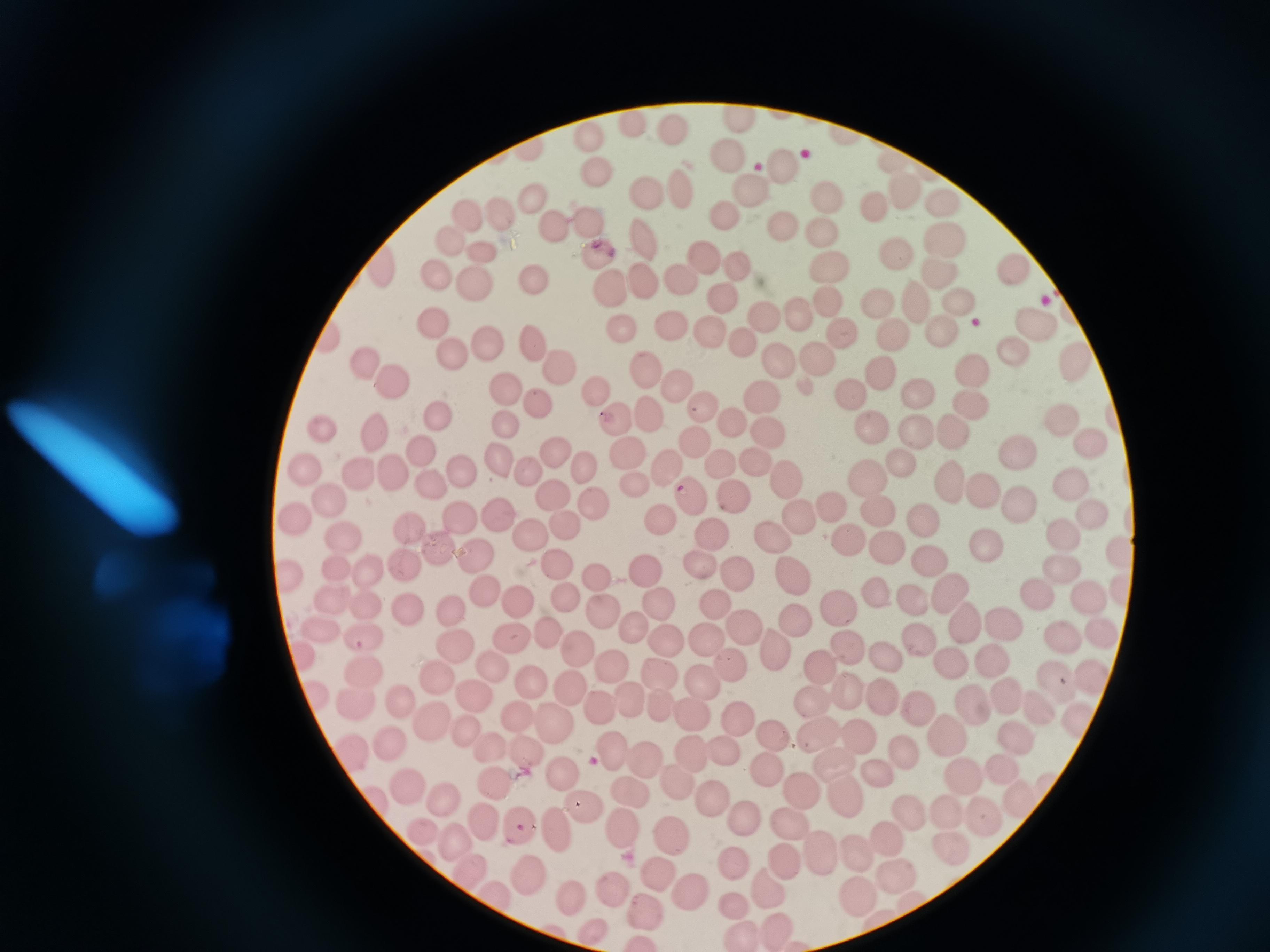

Approximate centers as [x, y] in pixels. Cell locations: [742, 117], [628, 125], [670, 127], [590, 133], [730, 157], [889, 159], [786, 165], [594, 173], [680, 188], [823, 190], [648, 192], [748, 193], [904, 196], [937, 197], [530, 200], [874, 205], [496, 214], [725, 216], [463, 218], [586, 223], [783, 223], [551, 224], [824, 230], [948, 237], [640, 239], [451, 240], [600, 254], [895, 255], [706, 256], [483, 257], [1017, 264], [382, 266], [826, 270], [435, 271], [738, 271], [943, 272], [677, 273], [470, 284], [538, 286], [645, 286], [611, 288], [723, 299], [956, 299], [827, 301], [918, 301], [874, 302], [795, 311], [771, 319], [672, 321], [1037, 321], [433, 325], [622, 325], [944, 329], [843, 331], [713, 332], [891, 334], [330, 340], [486, 341], [750, 341], [532, 345], [1012, 349], [447, 354], [778, 363], [819, 364], [369, 365], [971, 365], [641, 366], [1080, 366], [558, 369], [883, 373], [391, 379], [676, 382], [507, 387], [596, 388], [921, 391], [855, 394], [762, 396], [539, 404], [972, 407], [701, 411], [652, 413], [437, 417], [734, 417], [621, 419], [1063, 423], [507, 427], [920, 427], [873, 428], [952, 429], [329, 432], [375, 433], [766, 435], [692, 438], [1089, 440], [553, 449], [426, 451], [626, 452], [1017, 455], [500, 456], [582, 465], [759, 465], [905, 465], [668, 467], [723, 469], [308, 471], [394, 471], [523, 473], [466, 474], [361, 476], [870, 477], [784, 479], [952, 480], [435, 481], [1077, 484], [638, 485], [986, 492], [554, 494], [690, 495], [732, 497], [325, 499], [1018, 499], [594, 503], [833, 505], [880, 509], [800, 515], [1091, 515], [503, 518], [460, 519], [929, 520], [661, 521], [296, 522], [565, 528], [408, 530], [772, 533], [848, 535], [341, 537], [710, 538], [1066, 538], [536, 539], [436, 545], [890, 548], [1121, 549], [993, 552], [476, 556], [698, 560], [930, 560], [369, 564], [558, 564], [406, 566], [340, 567], [1064, 571], [289, 573], [643, 573], [735, 574], [793, 577], [595, 580], [1125, 589], [945, 591], [483, 593], [567, 594], [881, 596], [1094, 597], [332, 598], [366, 600], [1042, 601], [517, 604], [916, 604], [452, 605], [717, 605], [839, 606], [658, 607], [409, 610], [599, 610], [959, 622], [794, 623], [1000, 623], [744, 628], [549, 630], [633, 630], [318, 631], [1058, 634], [1096, 636], [361, 638], [914, 639], [451, 640], [511, 642], [704, 642], [664, 644], [574, 647], [844, 648], [772, 649], [301, 653], [881, 656], [953, 662], [732, 664], [819, 667], [993, 667], [491, 668], [614, 669], [365, 671], [1088, 675], [660, 676], [439, 677], [704, 679], [536, 682], [1057, 685], [849, 690], [570, 691], [471, 693], [879, 695], [317, 696], [1008, 696], [812, 700], [401, 703], [626, 703], [972, 703], [356, 704], [656, 704], [1038, 705], [600, 708], [916, 708], [691, 714], [517, 716], [735, 717], [433, 719], [1075, 721], [555, 724], [466, 729], [768, 735], [863, 736], [815, 737], [948, 737], [1017, 740], [386, 744], [491, 748], [352, 749], [531, 749], [688, 751], [907, 752], [608, 753], [726, 755], [834, 760], [644, 763], [768, 766], [1003, 767], [878, 769], [964, 773], [564, 774], [679, 782], [495, 784], [411, 785], [628, 789], [801, 789], [844, 798], [380, 800], [711, 801], [444, 803], [1023, 804], [585, 808], [983, 810], [951, 811], [909, 814], [745, 816], [485, 818], [515, 822], [790, 823], [554, 825], [623, 825], [422, 831], [673, 838], [452, 840], [886, 841], [950, 847], [857, 855], [785, 858], [819, 858], [465, 865], [731, 868], [527, 873], [664, 875], [897, 875], [613, 885], [768, 886], [686, 889], [576, 891], [856, 894], [496, 895], [734, 903], [649, 913], [777, 924], [597, 932], [739, 934]. Acquired by smartphone through the microscope eyepiece. Image is 1270×952 pixels. One field from this slide. Thin blood film. Giemsa-stained preparation.